Report the malaria status of this cell.
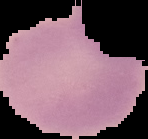

It is uninfected.

Summary:
  - Image type: cell region segmented out of the field of view; surrounding area masked to black
  - Image size: 148×139 pixels
  - Preparation: thin blood smear